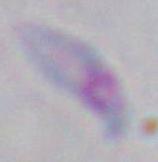

magnification = 1000x
modality = micrograph
identification = Toxoplasma gondii